Describe the morphology of the red blood cells.
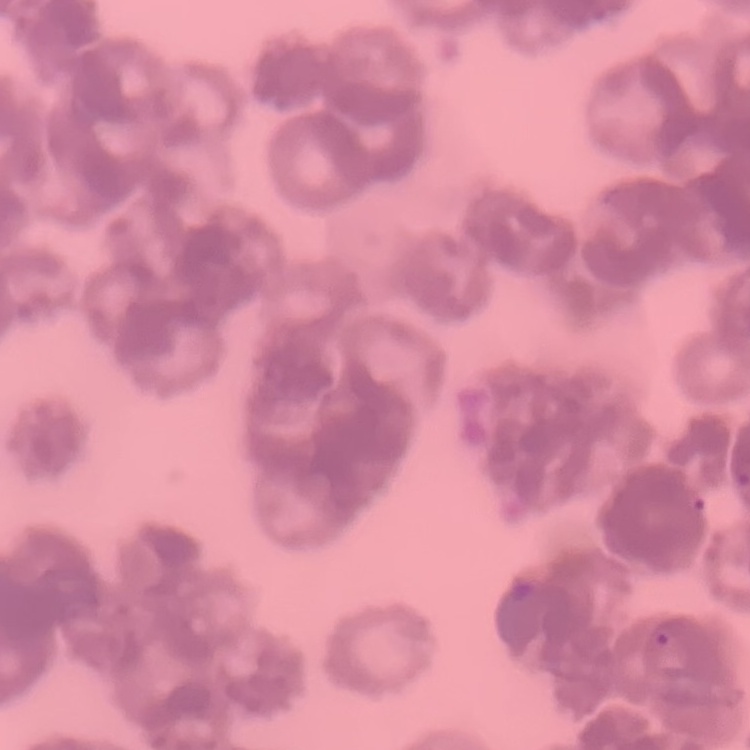

Rouleaux formation.

stain = Field's or Giemsa
preparation = thin blood film
image type = one tile cut from a larger photomicrograph